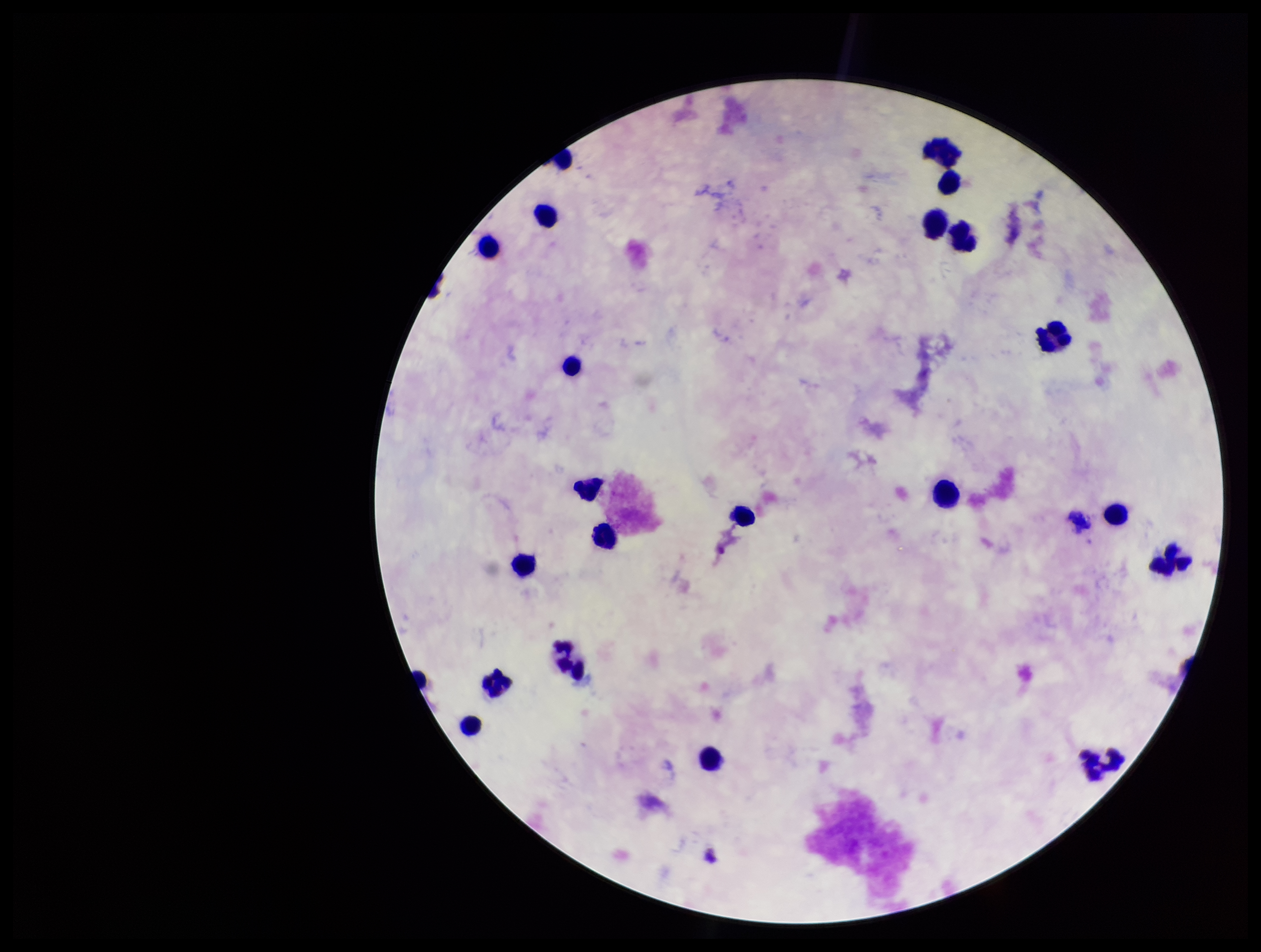

Leukocyte count: 21. Stained with Giemsa. Parasite count: 0. Single field of view. Image is 1261×952 pixels. Patient malaria status: negative. Smartphone photograph taken through the eyepiece of a microscope. Preparation: thick. Plasmodium parasites: none seen.